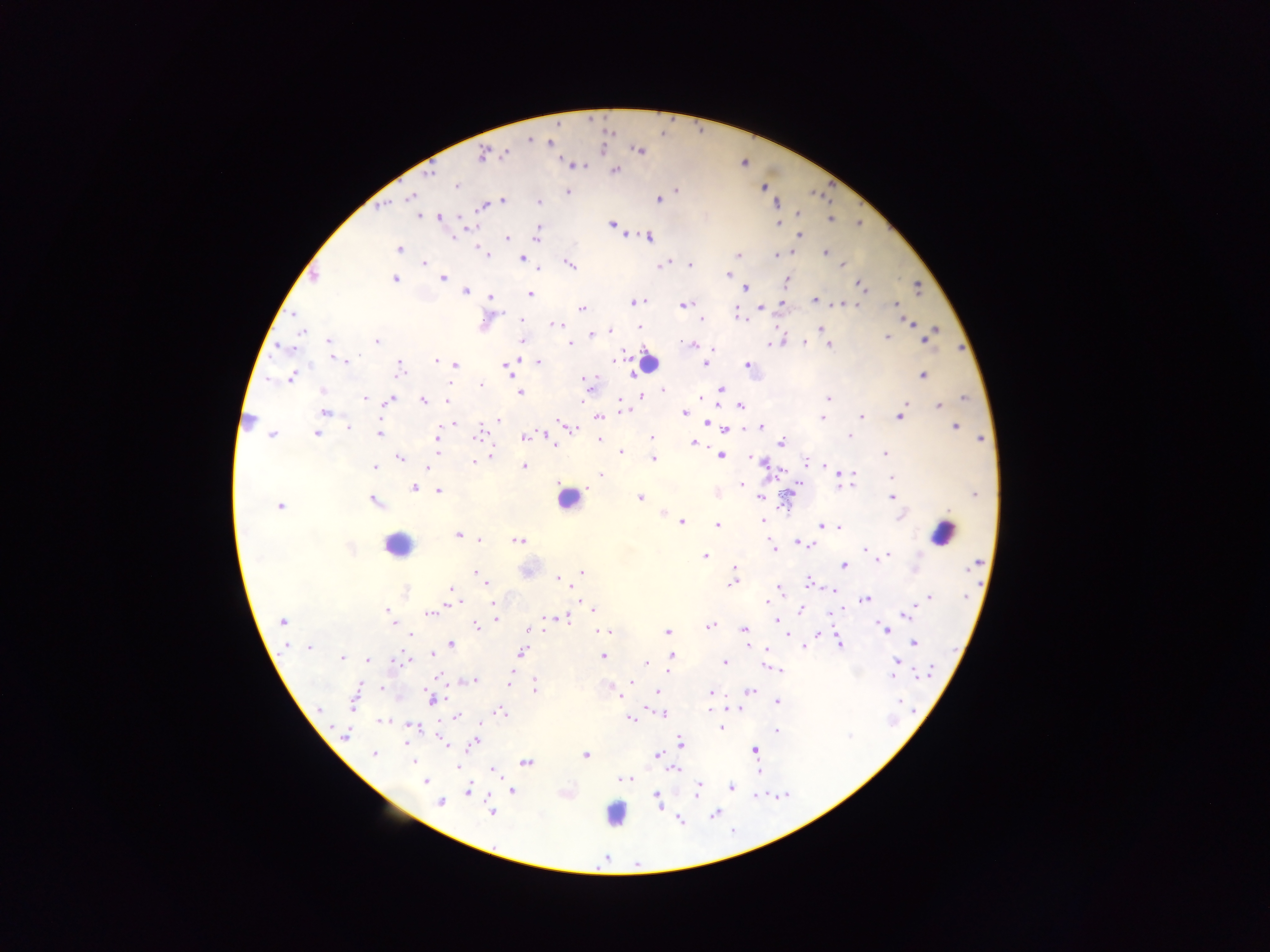

Approximate centers as x y in pixels. Plasmodium parasite locations: 609 132; 528 140; 551 143; 638 150; 505 153; 482 155; 572 165; 615 170; 429 172; 455 185; 676 191; 567 192; 410 197; 658 199; 503 202; 539 202; 775 203; 384 204; 482 205; 797 214; 417 216; 441 217; 829 218; 858 223; 612 224; 778 224; 472 226; 537 231; 798 234; 452 237; 536 237; 648 237; 506 238; 398 248; 825 252; 484 253; 738 256; 774 256; 486 258; 520 259; 568 263; 424 264; 663 264; 842 264; 688 265; 727 274; 314 275; 442 278; 393 279; 786 281; 860 285; 917 287; 745 288; 465 290; 530 294; 490 297; 814 300; 632 303; 855 303; 782 304; 843 304; 684 305; 896 305; 760 306; 582 308; 737 315; 521 320; 702 320; 911 323; 557 324; 639 327; 933 328; 819 329; 609 330; 302 331; 590 335; 926 336; 886 337; 328 340; 378 341; 522 341; 804 343; 568 344; 693 344; 767 345; 829 345; 285 347; 342 359; 612 360; 436 361; 536 361; 705 363; 455 365; 506 365; 748 365; 399 368; 510 369; 628 374; 922 376; 290 377; 586 379; 480 384; 449 385; 721 389; 663 390; 323 391; 518 393; 640 395; 365 397; 701 398; 829 399; 962 399; 389 400; 423 400; 447 400; 740 406; 938 406; 623 409; 324 412; 684 413; 900 415; 598 416; 860 416; 822 417; 249 420; 497 420; 707 423; 454 424; 760 425; 568 426; 954 426; 348 427; 726 430; 379 432; 316 433; 477 433; 272 435; 849 436; 524 438; 651 438; 599 439; 980 439; 436 440; 693 442; 781 443; 555 445; 438 452; 621 452; 490 454; 719 455; 885 455; 399 457; 653 458; 805 461; 473 462; 764 463; 821 465; 523 466; 376 467; 427 468; 840 471; 602 474; 837 476; 892 478; 799 482; 853 484; 742 485; 838 486; 413 487; 438 490; 717 492; 789 494; 975 494; 640 497; 759 497; 891 497; 374 500; 279 506; 663 511; 900 517; 763 521; 681 522; 717 525; 821 526; 837 527; 456 534; 479 540; 518 540; 798 542; 811 544; 773 550; 863 550; 888 553; 705 556; 881 557; 843 565; 734 566; 475 572; 583 572; 558 578; 734 582; 487 583; 807 583; 778 585; 451 588; 834 590; 406 591; 928 598; 865 599; 766 600; 493 602; 453 603; 843 606; 916 606; 387 609; 592 609; 800 610; 430 613; 904 613; 829 614; 552 617; 563 618; 773 619; 389 620; 496 620; 282 621; 775 622; 711 625; 477 629; 546 629; 884 629; 528 630; 744 630; 604 631; 667 632; 818 634; 410 635; 914 643; 452 644; 840 644; 287 647; 310 647; 804 647; 759 649; 765 650; 521 652; 671 653; 431 654; 602 656; 342 657; 367 661; 395 661; 896 661; 724 662; 645 663; 778 669; 667 670; 509 675; 916 676; 439 677; 891 677; 473 679; 632 681; 508 685; 381 687; 535 689; 617 691; 747 692; 656 693; 710 693; 431 699; 776 701; 353 702; 900 702; 729 709; 319 710; 500 712; 662 714; 456 717; 631 719; 383 720; 481 723; 411 725; 721 725; 720 728; 775 732; 346 735; 442 741; 474 743; 680 743; 754 750; 374 754; 657 754; 585 755; 414 761; 525 762; 456 767; 493 769; 673 769; 758 772; 622 779; 425 781; 698 786; 731 787; 510 790; 468 791; 695 794; 656 796; 439 802; 658 805; 491 812; 715 813; 679 819; 605 858. Leukocyte locations: 647 363; 569 498; 943 532; 396 545; 615 814. One field of view. Sample from Ghana. Thick blood film. Mobile-phone photograph taken through the microscope. Image is 1270×952 pixels.